Report the malaria status of this cell.
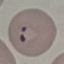
It is parasitized.

Automatically extracted cell patch, resized to 64 × 64 pixels. Acquired by smartphone through the microscope eyepiece. Thin blood smear. Giemsa-stained preparation.